Give the extent of all Plasmodium ovale-infected red blood cells.
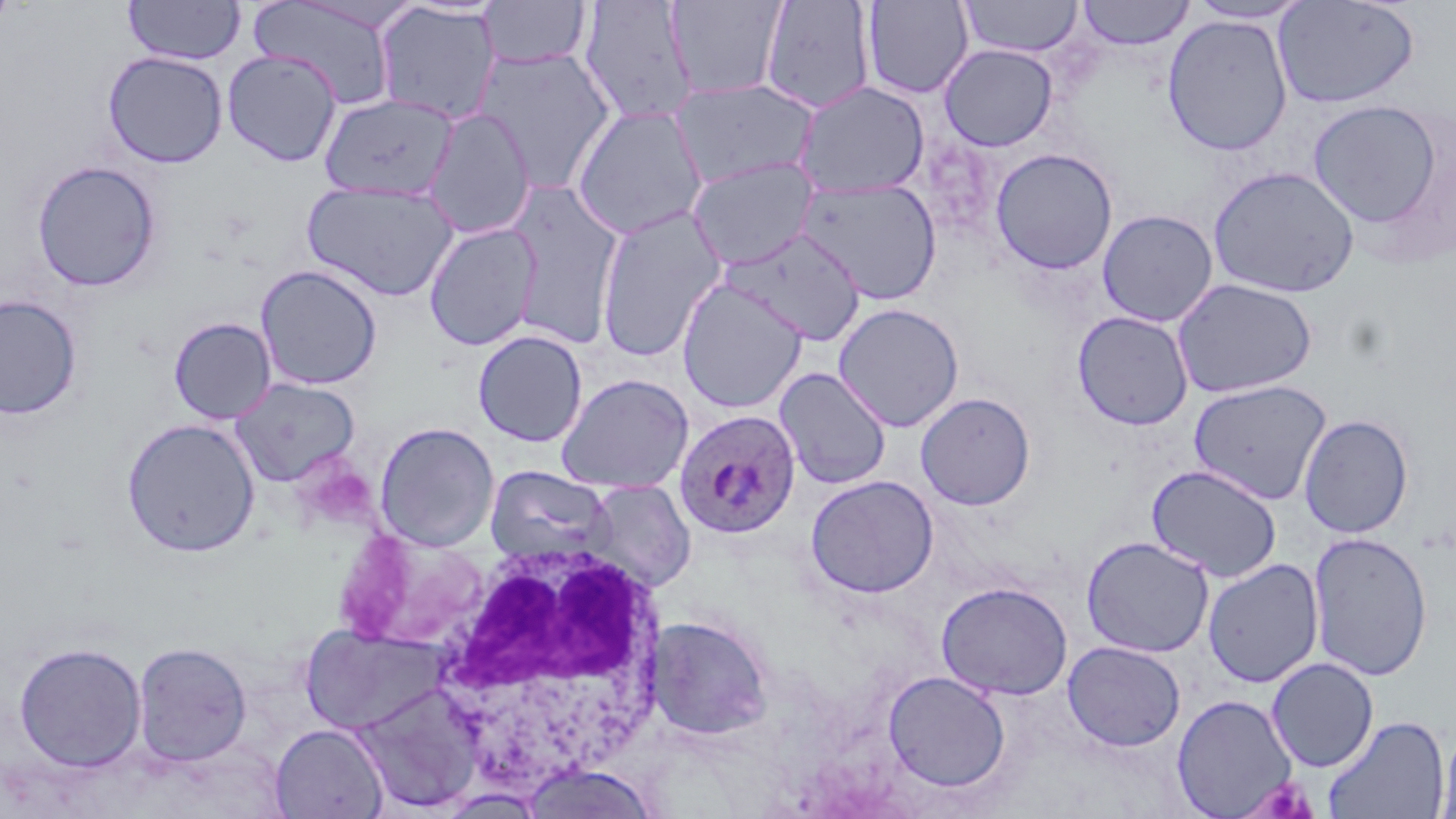

Approximate bounding boxes as (x1,y1)-(x2,y2) corner pairs in pixels.
Plasmodium ovale-infected red blood cells: (673,409)-(802,539).

slide-level diagnosis = Plasmodium ovale
image size = 1456×819 pixels
magnification = 1000x
preparation = thin blood smear
field of view = one of a larger specimen
stain = May-Grünwald-Giemsa
uninfected red blood cell locations (subset) = approximate bounding boxes as (x1,y1)-(x2,y2) corner pairs in pixels: (122,0)-(245,65), (578,0)-(698,127), (861,0)-(973,99), (958,0)-(1083,57), (1272,0)-(1420,109), (249,1)-(401,110), (477,1)-(592,69), (665,1)-(788,99), (760,1)-(876,114), (1076,1)-(1195,50), (1185,1)-(1311,24), (374,4)-(501,125), (1161,14)-(1293,156), (474,44)-(618,191), (939,44)-(1058,151), (222,49)-(342,167), (102,51)-(228,168), (670,78)-(819,190), (794,81)-(930,198), (319,92)-(459,200), (1307,100)-(1445,229), (571,104)-(709,240), (422,108)-(537,239), (989,148)-(1118,275), (687,156)-(820,270), (31,160)-(161,292), (1207,165)-(1361,299), (796,177)-(943,305), (301,180)-(458,301), (503,182)-(626,349), (595,206)-(728,362), (1096,209)-(1218,327), (424,222)-(542,352), (719,228)-(866,345), (255,264)-(382,391), (676,278)-(808,414), (1171,278)-(1318,399), (0,295)-(82,420), (833,302)-(964,432), (1072,311)-(1194,430), (168,317)-(276,424), (472,329)-(588,447), (775,367)-(891,490), (556,373)-(694,494), (229,377)-(361,487), (1188,379)-(1333,505), (915,392)-(1036,510), (1299,414)-(1414,539), (121,418)-(260,557), (374,422)-(500,551), (1146,464)-(1282,582), (484,465)-(616,565), (806,475)-(939,598), (582,479)-(696,593), (1308,532)-(1433,682), (1080,535)-(1214,658), (1203,559)-(1324,688), (936,581)-(1073,700), (645,615)-(774,740), (300,622)-(448,736), (13,641)-(148,773), (1063,641)-(1185,752), (132,642)-(253,767), (1267,657)-(1379,772), (882,670)-(1011,793), (353,682)-(485,812), (1171,694)-(1298,818), (1323,714)-(1449,819), (1435,721)-(1456,819), (269,724)-(389,818), (518,762)-(661,819)
modality = optical microscopy